Identify the preparation type.
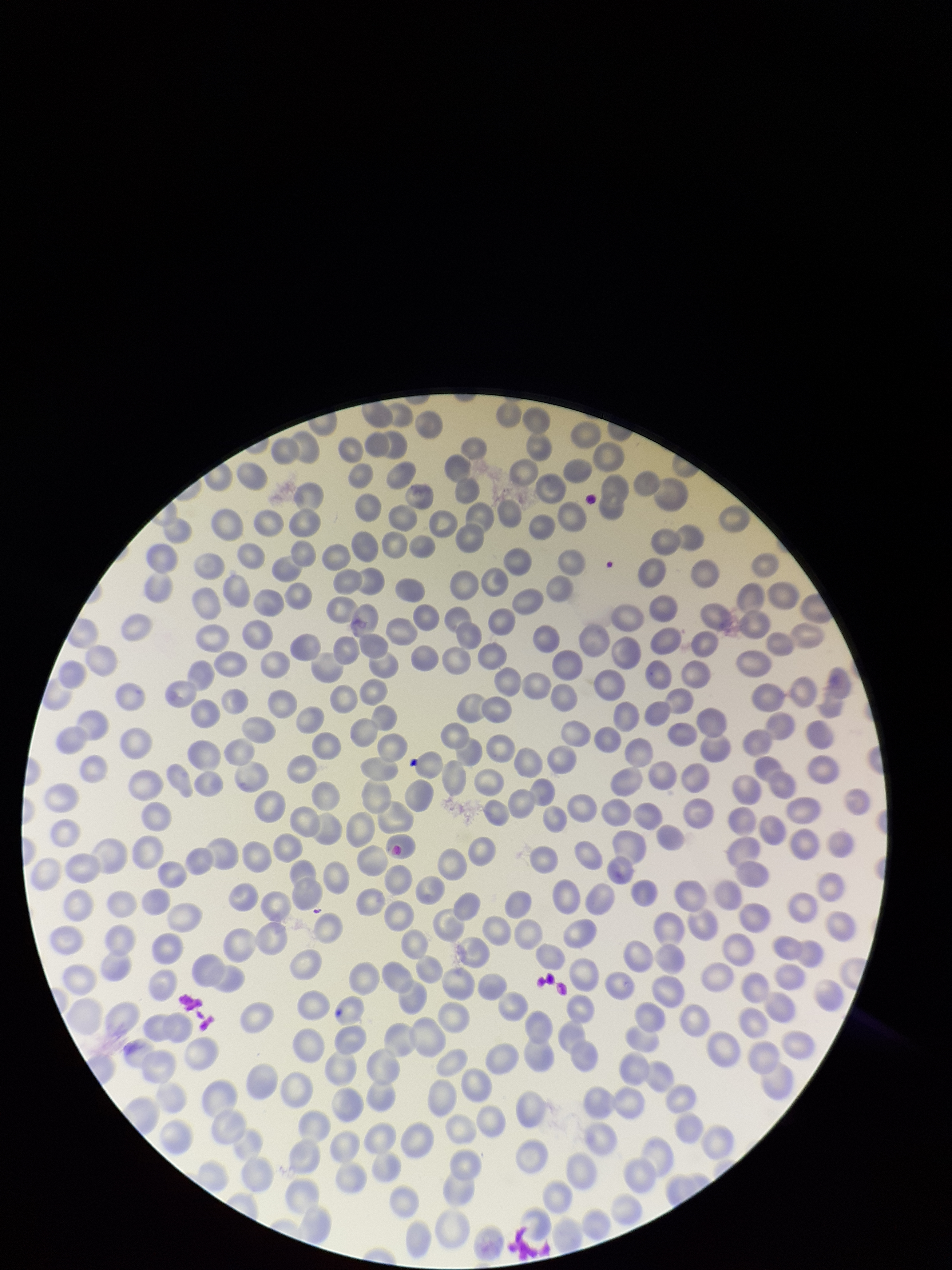
Thin.

{
  "stain": "Giemsa",
  "red_blood_cell_count": 279,
  "image_size": "952×1270 pixels",
  "parasitized_red_blood_cell_count": 0,
  "patient_malaria_status": "negative",
  "capture": "smartphone photograph through the microscope eyepiece",
  "parasitized_red_blood_cells": "none seen",
  "field_of_view": "one from this slide"
}